Assess the morphology of the red blood cells.
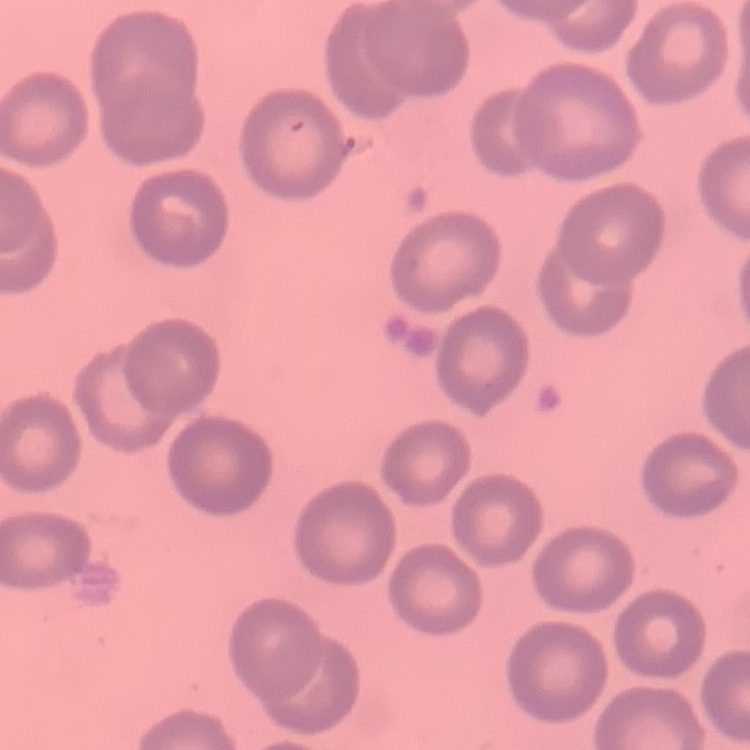
They show no rouleaux formation.

One tile cut from a larger photomicrograph. Thin peripheral smear. Stained with either Field's or Giemsa.